Assess the morphology of the red blood cells.
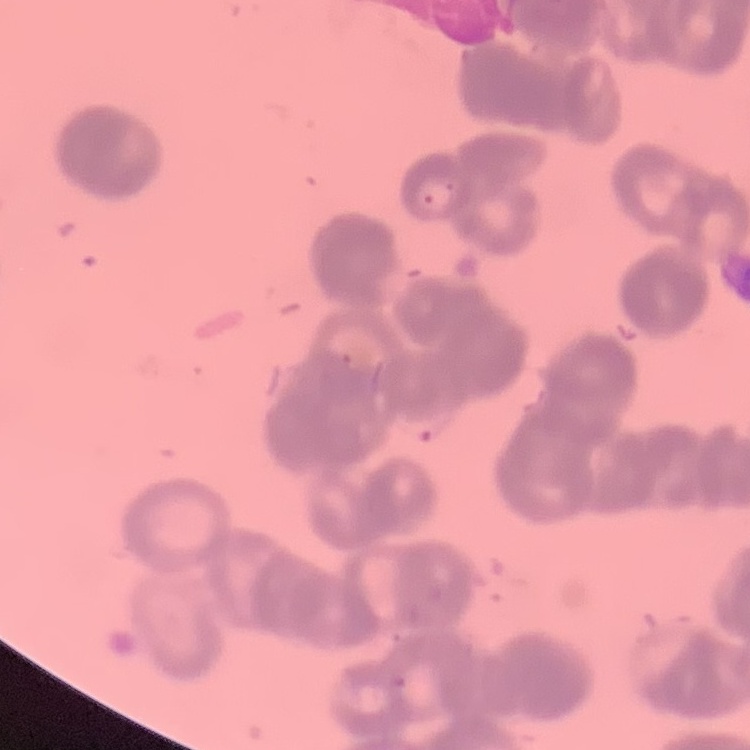
Rouleaux formation.

Summary:
  - Preparation: thin blood film
  - Stain: Field's or Giemsa
  - Image type: square crop of a larger photomicrograph